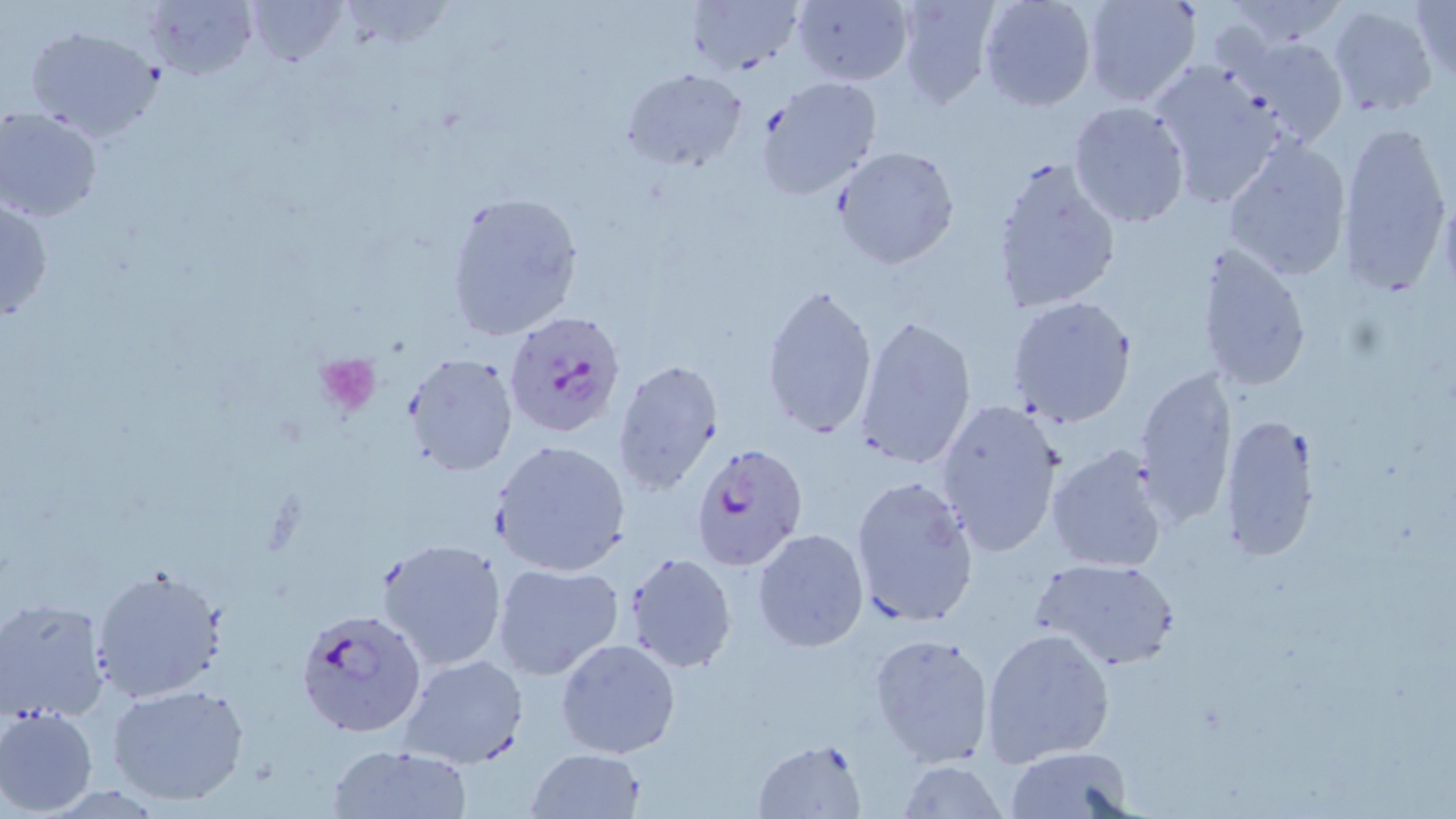
Approximate bounding boxes as named x1/y1/x2/y2 corners in pixels. Platelet locations: (x1=315, y1=353, x2=382, y2=416). Uninfected red blood cell locations: (x1=244, y1=0, x2=347, y2=69), (x1=894, y1=0, x2=1000, y2=108), (x1=977, y1=0, x2=1098, y2=112), (x1=1081, y1=0, x2=1200, y2=107), (x1=1221, y1=0, x2=1348, y2=52), (x1=1409, y1=0, x2=1455, y2=88), (x1=144, y1=1, x2=255, y2=79), (x1=687, y1=1, x2=802, y2=73), (x1=790, y1=1, x2=914, y2=86), (x1=1326, y1=4, x2=1439, y2=118), (x1=25, y1=24, x2=165, y2=143), (x1=1228, y1=34, x2=1351, y2=149), (x1=1147, y1=58, x2=1290, y2=208), (x1=620, y1=68, x2=749, y2=171), (x1=756, y1=75, x2=882, y2=199), (x1=1067, y1=100, x2=1192, y2=229), (x1=0, y1=106, x2=105, y2=222), (x1=1336, y1=122, x2=1453, y2=297), (x1=1220, y1=134, x2=1355, y2=283), (x1=832, y1=145, x2=959, y2=270), (x1=988, y1=155, x2=1122, y2=318), (x1=0, y1=192, x2=54, y2=326), (x1=443, y1=192, x2=584, y2=342), (x1=1196, y1=241, x2=1314, y2=394), (x1=759, y1=281, x2=880, y2=445), (x1=1007, y1=296, x2=1139, y2=430), (x1=853, y1=313, x2=978, y2=472), (x1=403, y1=353, x2=519, y2=476), (x1=611, y1=357, x2=727, y2=495), (x1=1134, y1=365, x2=1237, y2=530), (x1=935, y1=396, x2=1068, y2=559), (x1=1220, y1=412, x2=1319, y2=563), (x1=491, y1=439, x2=632, y2=577), (x1=1044, y1=441, x2=1172, y2=574), (x1=850, y1=473, x2=979, y2=627), (x1=753, y1=528, x2=869, y2=651), (x1=376, y1=537, x2=510, y2=672), (x1=623, y1=553, x2=737, y2=674), (x1=1031, y1=555, x2=1181, y2=671), (x1=493, y1=563, x2=623, y2=682), (x1=91, y1=566, x2=229, y2=701), (x1=1, y1=599, x2=113, y2=724), (x1=981, y1=627, x2=1116, y2=765), (x1=868, y1=632, x2=996, y2=769), (x1=555, y1=637, x2=679, y2=759), (x1=398, y1=652, x2=527, y2=768), (x1=105, y1=682, x2=251, y2=807), (x1=1, y1=705, x2=99, y2=815), (x1=753, y1=738, x2=867, y2=818), (x1=325, y1=744, x2=470, y2=818), (x1=1006, y1=746, x2=1135, y2=818), (x1=525, y1=748, x2=647, y2=819), (x1=898, y1=759, x2=1007, y2=817). Plasmodium falciparum-infected red blood cell locations: (x1=502, y1=311, x2=628, y2=438), (x1=688, y1=443, x2=810, y2=571), (x1=294, y1=606, x2=426, y2=739). Slide-level diagnosis: Plasmodium falciparum. Optical microscopy. May-Grünwald-Giemsa stain. 1000x magnification. One field of a larger specimen. Image is 1456×819 pixels. Thin blood smear.